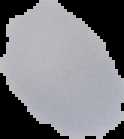 Segmented cell region on a black background. Image is 124×139 pixels. From a thin blood smear. Result: no Plasmodium parasites detected.